Assess the morphology of the erythrocytes.
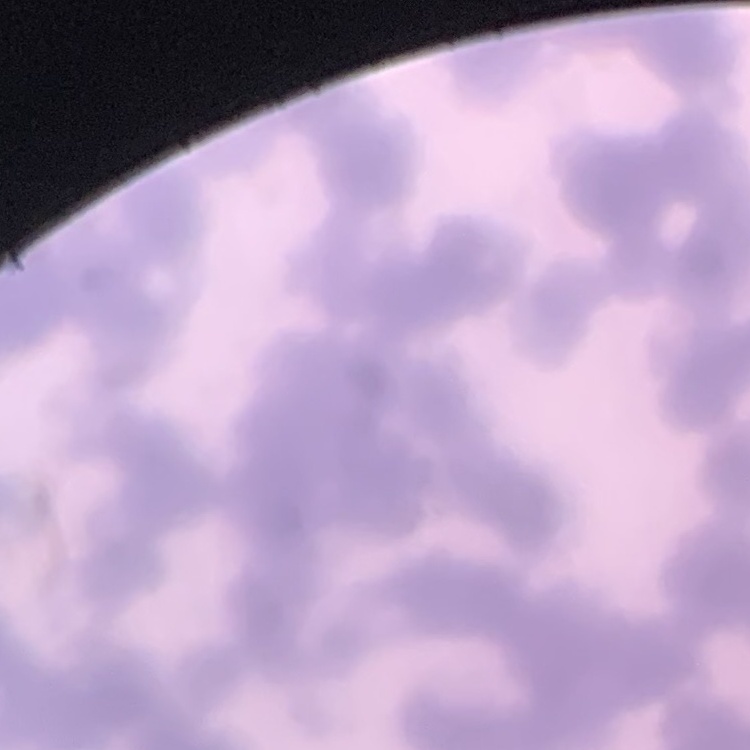

They show rouleaux formation.

Thin blood smear. One tile cut from a larger photomicrograph. Field's or Giemsa stain.